Report the malaria status of this cell.
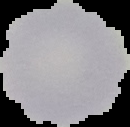
Uninfected.

image size = 130×127 pixels
preparation = thin blood smear
image type = segmented cell region with the area outside set to black